Outline platelets.
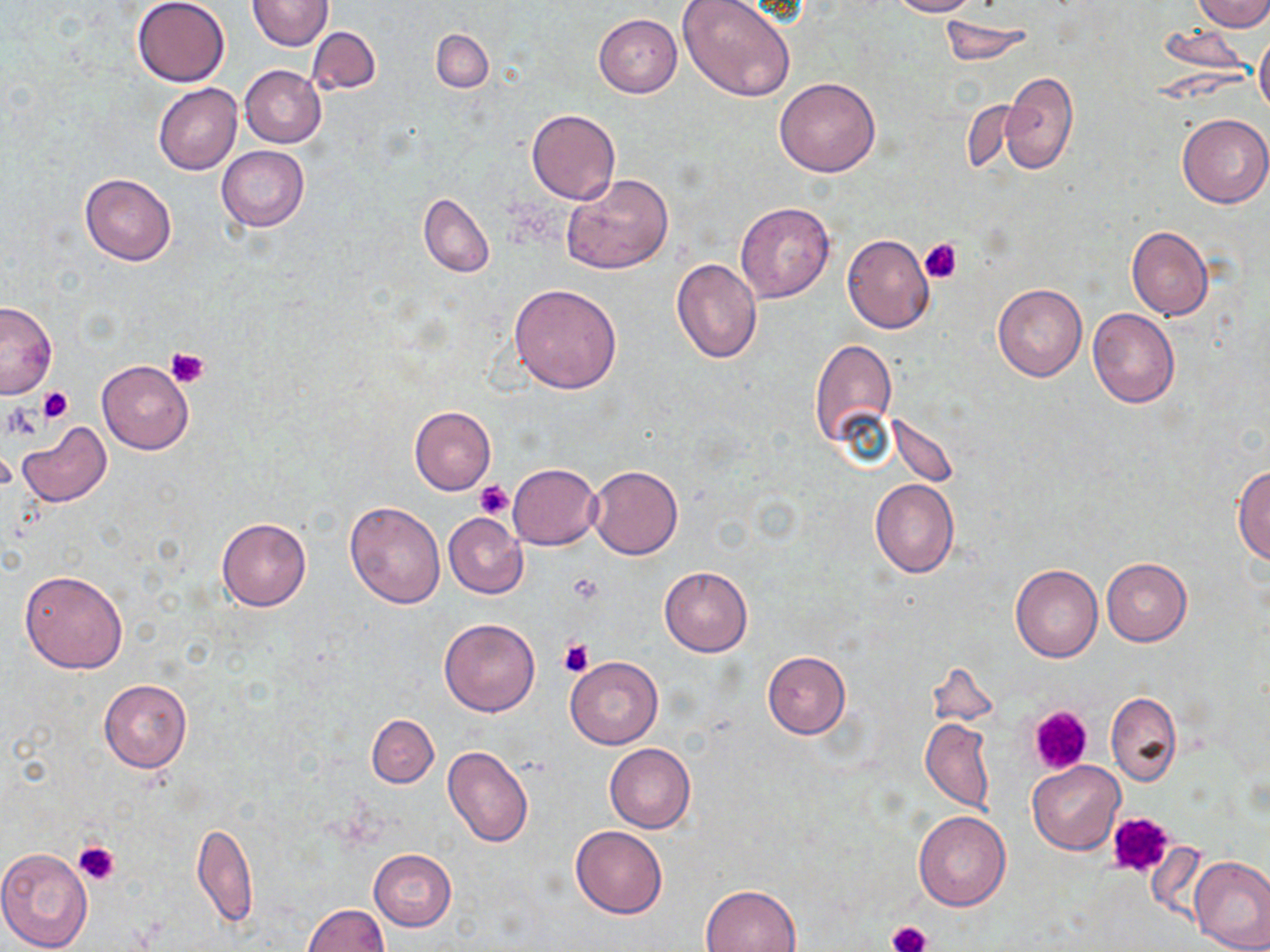
Approximate bounding boxes as (x1,y1)-(x2,y2) corner pairs in pixels.
Platelets: (918,239)-(963,283), (165,346)-(209,389), (39,387)-(72,423), (3,403)-(44,441), (476,480)-(514,520), (559,639)-(593,678), (1026,704)-(1094,777), (1106,811)-(1174,879), (73,841)-(119,884), (889,921)-(930,950).

Uninfected red blood cell locations: (131,0)-(230,86), (246,0)-(334,50), (677,0)-(797,105), (887,0)-(976,17), (1194,0)-(1270,32), (594,14)-(682,97), (938,17)-(1035,66), (1157,24)-(1255,80), (307,26)-(380,95), (431,29)-(492,91), (1254,30)-(1270,117), (239,66)-(326,147), (997,72)-(1079,175), (774,77)-(880,177), (154,83)-(242,176), (526,110)-(620,204), (1177,113)-(1270,207), (216,146)-(310,230), (562,173)-(673,273), (80,174)-(176,264), (418,192)-(494,277), (735,201)-(834,302), (1127,226)-(1214,321), (842,234)-(935,333), (670,258)-(763,363), (993,283)-(1087,382), (509,284)-(622,392), (0,300)-(57,398), (1087,307)-(1180,408), (808,336)-(897,452), (97,361)-(194,454), (410,406)-(496,495), (888,412)-(959,485), (16,422)-(112,508), (588,464)-(683,559), (508,465)-(600,549), (1232,465)-(1270,565), (870,480)-(960,577), (345,501)-(446,609), (444,512)-(527,598), (216,517)-(311,611), (1101,557)-(1191,645), (1010,564)-(1102,662), (659,565)-(753,656), (19,569)-(128,674), (439,618)-(540,716), (762,652)-(850,738), (564,656)-(663,749), (926,662)-(1001,732), (98,679)-(192,772), (1106,692)-(1182,788), (367,714)-(438,787), (921,718)-(995,814), (604,743)-(696,833), (442,746)-(534,849), (1028,759)-(1124,854), (913,811)-(1011,911), (192,823)-(258,929), (571,825)-(668,919), (0,847)-(93,951), (369,848)-(455,929), (1189,855)-(1270,952), (701,884)-(799,952), (303,904)-(388,952). Slide-level diagnosis: negative for blood parasites. Thin blood smear. Light microscopy. One field of a larger specimen. May-Grünwald-Giemsa-stained preparation. Image is 1270×952 pixels. Captured at 1000x magnification.